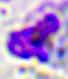

{
  "identification": "leukocyte",
  "modality": "photomicrograph",
  "magnification": "400x"
}